Locate the cells, classifying each as a parasitized RBC, an uninfected RBC, or a WBC.
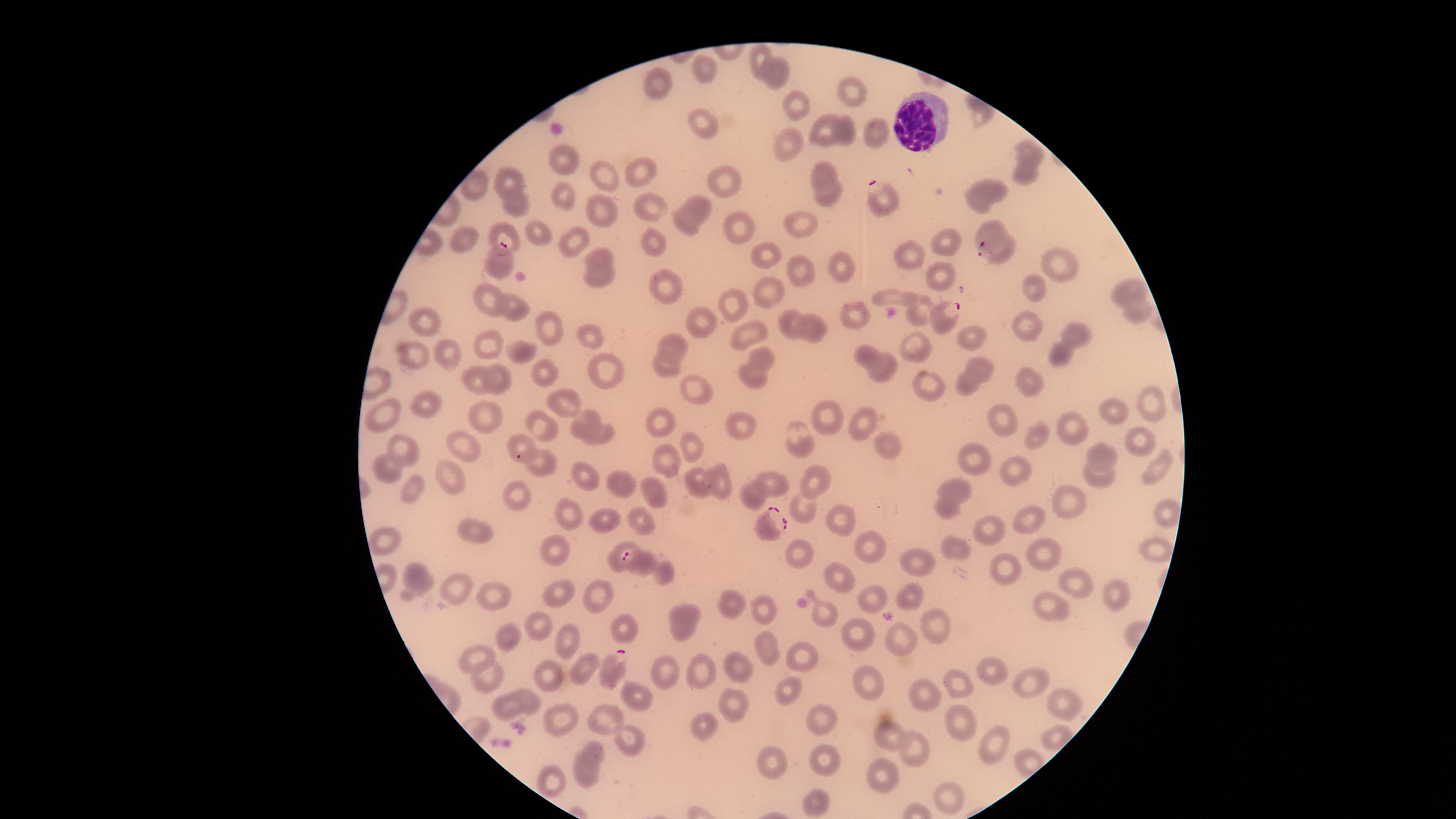

Approximate marker points as (x, y) in pixels.
Parasitized RBCs: (884, 202), (988, 236), (498, 261), (944, 319), (769, 521), (639, 561), (640, 562), (617, 665).
Uninfected RBCs: (707, 71), (660, 87), (848, 88), (699, 120), (822, 128), (846, 132), (871, 133), (1029, 149), (566, 164), (639, 171), (825, 173), (1028, 174), (603, 175), (510, 179), (724, 182), (476, 187), (984, 192), (563, 194), (825, 196), (646, 203), (704, 205), (512, 207), (601, 211), (801, 222), (684, 223), (537, 226), (501, 230), (734, 232), (465, 237), (656, 238), (572, 241), (942, 242), (907, 252), (763, 253), (1005, 254), (598, 257), (842, 263), (1057, 263), (799, 271), (942, 274), (597, 276), (1037, 283), (771, 285), (666, 286), (1127, 289), (488, 293), (893, 295), (736, 303), (858, 305), (518, 306), (919, 309), (1136, 314), (424, 318), (701, 319), (787, 323), (1028, 326), (816, 327), (748, 328), (548, 330), (587, 332), (966, 336), (1075, 336), (678, 342), (487, 343), (918, 345), (519, 353), (763, 353), (1060, 353), (863, 355), (446, 357), (415, 358), (667, 363), (979, 368), (605, 369), (546, 371), (888, 371), (499, 375), (750, 375), (1025, 378), (476, 382), (929, 385), (967, 385), (697, 390), (1149, 401), (424, 404), (563, 405), (387, 409), (487, 413), (1117, 413), (827, 415), (862, 415), (662, 418), (1006, 418), (581, 421), (540, 422), (743, 423), (1068, 423), (601, 432), (1034, 436), (519, 439), (1137, 439), (458, 440), (406, 442), (796, 442), (692, 443), (888, 446), (1103, 451), (978, 457), (539, 461), (667, 461), (386, 464), (1152, 468), (1013, 472), (453, 475), (588, 477), (818, 477), (1096, 478), (619, 480), (718, 482), (774, 482), (698, 485), (957, 485), (415, 487), (751, 494), (513, 495), (652, 497), (1070, 502), (942, 507), (803, 510), (1166, 511), (573, 512), (840, 512), (1031, 518), (608, 520), (644, 521), (987, 526), (478, 529), (550, 543), (384, 546), (625, 546), (874, 546), (955, 547), (1041, 547), (1155, 547), (799, 552), (917, 560), (1006, 569), (663, 572), (419, 575), (838, 577), (1080, 578), (454, 586), (555, 592), (499, 593), (600, 594), (913, 594), (1115, 597), (873, 598), (762, 606), (733, 609), (1047, 609), (819, 610), (684, 616), (533, 620), (935, 620), (625, 628), (860, 633), (570, 636), (507, 640), (897, 640), (763, 645), (798, 655), (478, 661), (735, 664), (702, 669), (583, 670), (992, 670), (666, 671), (548, 673), (489, 675), (958, 681), (1026, 682), (867, 683), (789, 689), (926, 692), (637, 694), (1063, 699), (529, 700), (726, 701), (509, 707), (558, 716), (609, 716), (818, 718), (958, 721), (702, 723), (888, 734), (1053, 734), (627, 736), (997, 746), (917, 748), (595, 749), (826, 755), (774, 758), (883, 769), (585, 773), (550, 779), (820, 796), (951, 796).
WBCs: (918, 121).

Circular visible region. Species: Plasmodium falciparum. Thin blood smear. One field of view of the specimen. Giemsa-stained preparation. Image is 1456×819 pixels. Smartphone photograph through the microscope eyepiece.